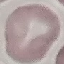
Result: no malaria parasites seen. Automatically extracted cell patch, resized to 64 × 64 pixels. Acquired by smartphone through the microscope eyepiece. Thin smear of blood. Giemsa-stained preparation.